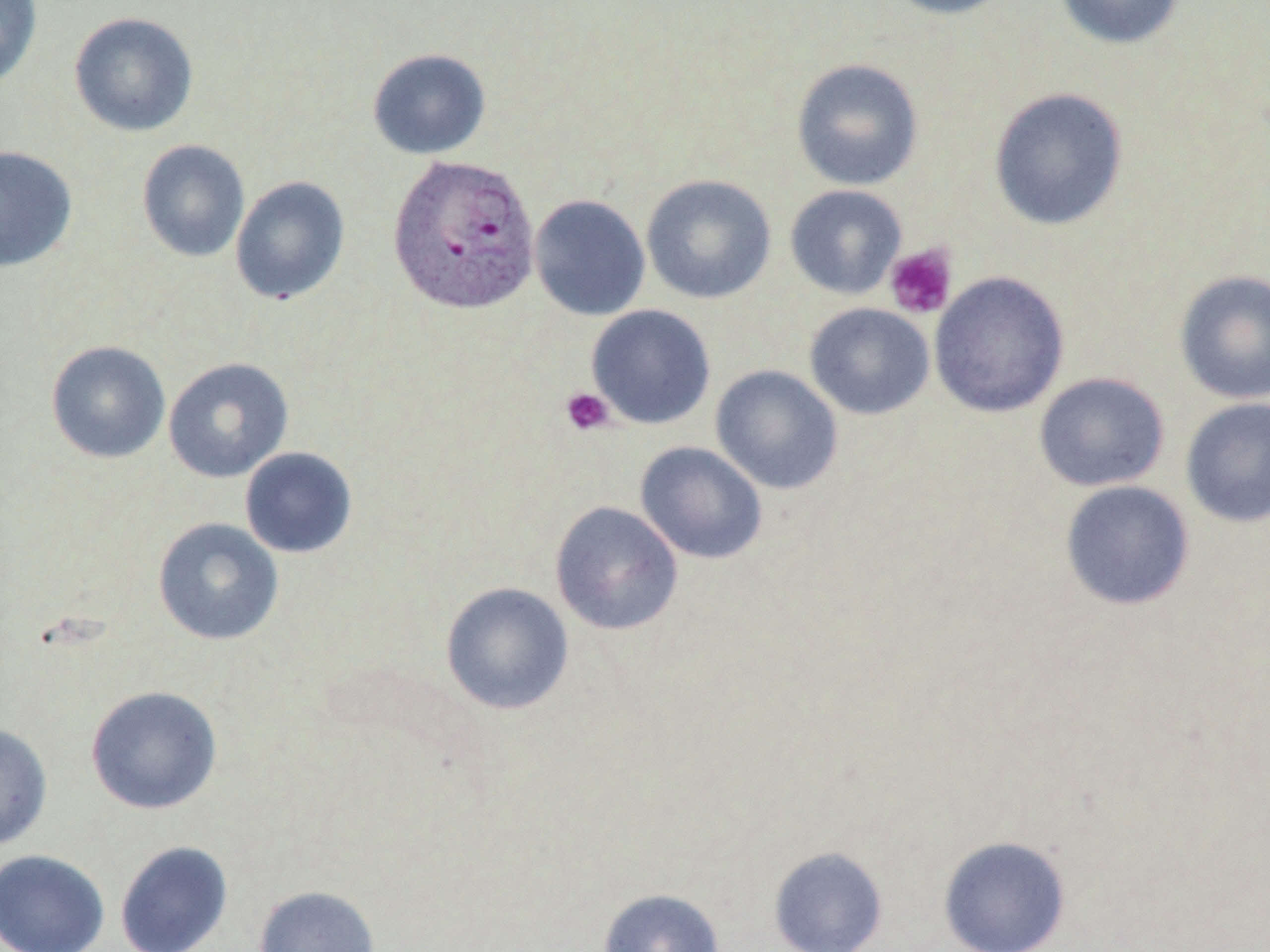

Approximate bounding boxes as [x1, y1, x2, y2] in pixels. Uninfected red blood cell locations: [0, 0, 43, 89], [879, 0, 1018, 20], [1054, 0, 1186, 50], [68, 12, 199, 137], [367, 48, 491, 159], [791, 58, 924, 191], [988, 87, 1129, 232], [136, 140, 250, 263], [0, 145, 78, 273], [641, 174, 777, 304], [230, 175, 351, 305], [785, 185, 907, 299], [529, 194, 651, 321], [1174, 269, 1270, 405], [928, 271, 1070, 418], [805, 303, 935, 420], [586, 304, 716, 429], [46, 340, 170, 463], [163, 357, 293, 482], [710, 365, 843, 495], [1033, 372, 1170, 492], [1180, 397, 1270, 528], [634, 441, 768, 564], [239, 447, 358, 559], [1059, 480, 1195, 611], [549, 501, 684, 636], [153, 517, 284, 646], [440, 581, 574, 715], [85, 685, 222, 814], [0, 723, 53, 850], [937, 835, 1072, 951], [114, 840, 233, 952], [768, 846, 889, 952], [0, 849, 110, 952], [253, 885, 380, 952], [597, 888, 725, 952]. Plasmodium ovale-infected red blood cell locations: [387, 155, 541, 315]. Platelet locations: [884, 243, 957, 319], [561, 386, 615, 436]. Slide-level diagnosis: Plasmodium ovale. Optical microscopy. Thin blood film. Image is 1270×952 pixels. One field of a larger specimen. 1000x magnification. May-Grünwald-Giemsa stain.